Locate every Plasmodium parasite.
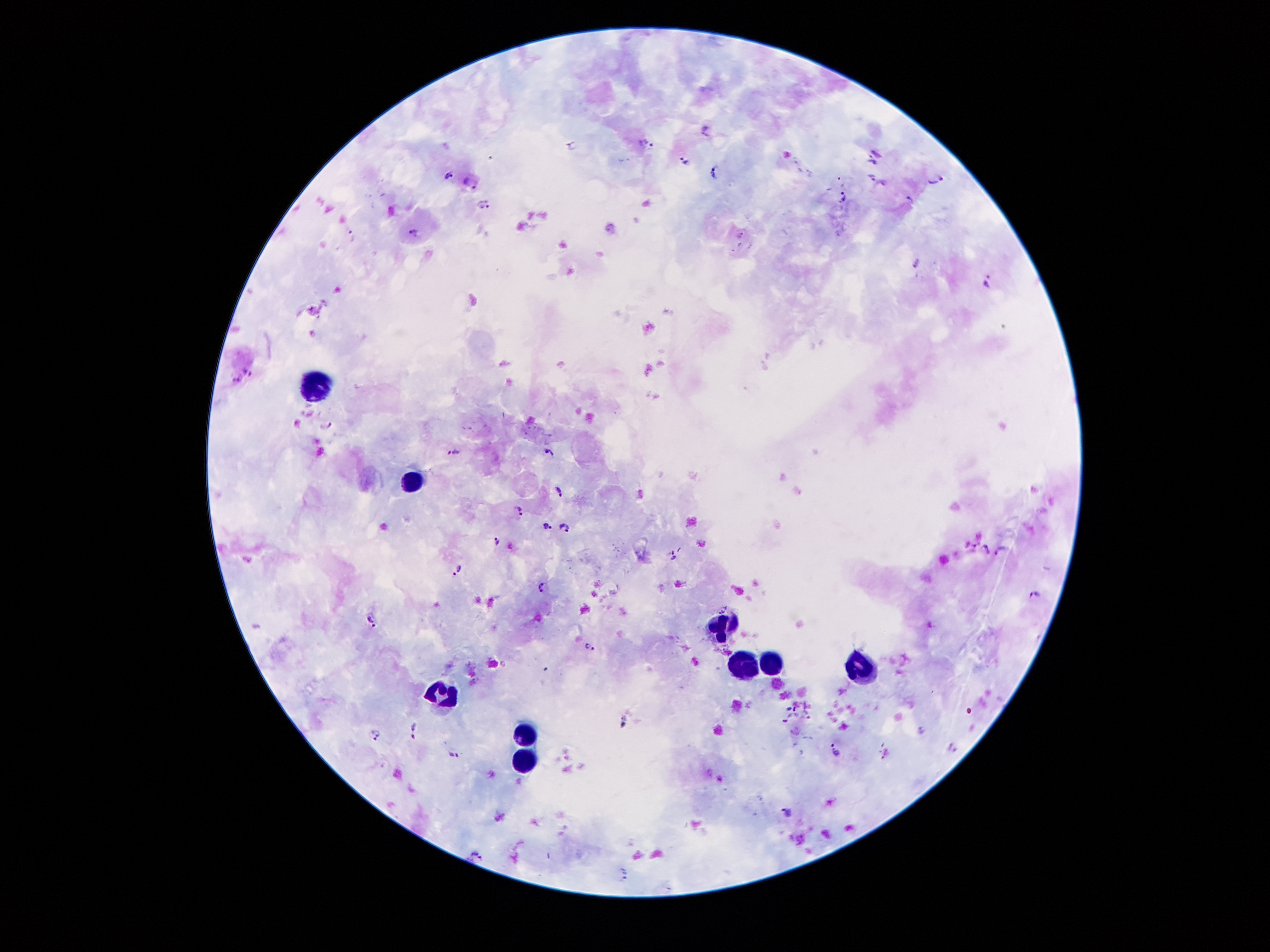
Approximate centers as (x, y) in pixels.
Plasmodium parasites: (706, 126), (646, 144), (876, 151), (684, 160), (871, 162), (715, 170), (448, 174), (871, 177), (935, 178), (469, 179), (884, 185), (843, 199), (910, 201), (483, 206), (412, 232), (351, 237), (917, 263), (987, 278), (246, 367), (236, 381), (327, 424), (548, 450), (454, 452), (559, 490), (797, 491), (519, 511), (547, 527), (567, 528), (497, 541), (972, 548), (985, 549), (1001, 551), (672, 556), (458, 568), (543, 586), (1033, 595), (369, 621), (588, 645), (790, 708), (807, 711), (410, 725), (920, 730), (377, 736), (834, 748), (954, 749), (885, 755), (454, 757), (787, 810), (476, 853), (623, 870).

{
  "image_size": "1270×952 pixels",
  "leukocyte_locations": "approximate centers as (x, y) in pixels: (312, 383), (411, 485), (724, 626), (772, 656), (736, 661), (862, 666), (442, 692), (523, 733), (522, 765)",
  "magnification": "100x",
  "field_of_view": "one from this slide",
  "capture": "smartphone camera through the microscope eyepiece",
  "patient_malaria_status": "positive for Plasmodium falciparum",
  "preparation": "thick blood film",
  "stain": "Giemsa"
}